Outline each Plasmodium falciparum-infected red blood cell.
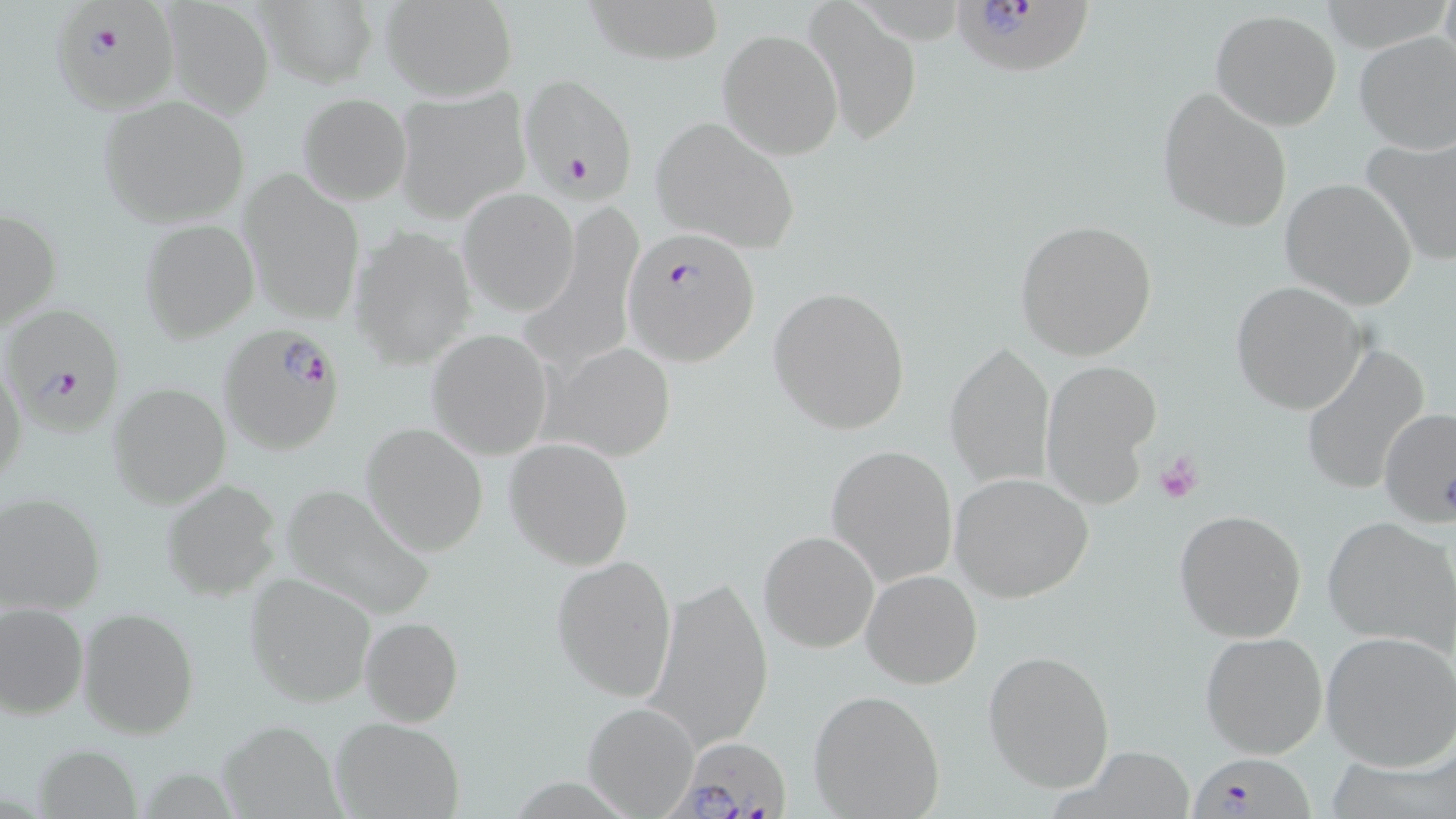

Approximate bounding boxes as named x1/y1/x2/y2 corners in pixels.
Plasmodium falciparum-infected red blood cells: (x1=55, y1=2, x2=186, y2=121), (x1=949, y1=4, x2=1094, y2=78), (x1=528, y1=78, x2=635, y2=210), (x1=622, y1=226, x2=762, y2=368), (x1=4, y1=306, x2=127, y2=427), (x1=217, y1=324, x2=346, y2=455), (x1=660, y1=735, x2=792, y2=819), (x1=1191, y1=752, x2=1309, y2=819).

slide_level_diagnosis: Plasmodium falciparum
stain: May-Grünwald-Giemsa
modality: light microscopy
image_size: 1456×819 pixels
magnification: 1000x
field_of_view: one of a larger specimen
preparation: thin blood film
uninfected_red_blood_cell_locations: 'approximate bounding boxes as named x1/y1/x2/y2 corners in pixels: (x1=161, y1=0, x2=275, y2=118), (x1=583, y1=0, x2=725, y2=65), (x1=379, y1=1, x2=518, y2=100), (x1=804, y1=1, x2=924, y2=146), (x1=252, y1=2, x2=377, y2=87), (x1=1210, y1=8, x2=1342, y2=131), (x1=718, y1=28, x2=841, y2=159), (x1=1353, y1=31, x2=1456, y2=156), (x1=1157, y1=87, x2=1293, y2=233), (x1=394, y1=89, x2=530, y2=223), (x1=297, y1=92, x2=411, y2=206), (x1=98, y1=96, x2=248, y2=229), (x1=650, y1=115, x2=800, y2=253), (x1=1362, y1=133, x2=1456, y2=268), (x1=238, y1=171, x2=366, y2=325), (x1=1280, y1=178, x2=1417, y2=309), (x1=458, y1=187, x2=579, y2=315), (x1=1, y1=205, x2=61, y2=335), (x1=1014, y1=218, x2=1158, y2=362), (x1=138, y1=220, x2=259, y2=342), (x1=350, y1=225, x2=477, y2=367), (x1=1230, y1=281, x2=1368, y2=414), (x1=768, y1=286, x2=911, y2=435), (x1=427, y1=330, x2=554, y2=458), (x1=945, y1=341, x2=1055, y2=487), (x1=544, y1=342, x2=677, y2=464), (x1=1301, y1=342, x2=1433, y2=497), (x1=0, y1=354, x2=27, y2=495), (x1=1043, y1=362, x2=1163, y2=506), (x1=107, y1=381, x2=231, y2=509), (x1=1378, y1=407, x2=1456, y2=527), (x1=360, y1=422, x2=488, y2=555), (x1=505, y1=437, x2=635, y2=570), (x1=826, y1=444, x2=957, y2=587), (x1=950, y1=472, x2=1094, y2=601), (x1=161, y1=479, x2=282, y2=601), (x1=279, y1=483, x2=431, y2=620), (x1=1, y1=492, x2=105, y2=615), (x1=1173, y1=508, x2=1307, y2=642), (x1=1322, y1=517, x2=1456, y2=651), (x1=759, y1=530, x2=879, y2=653), (x1=553, y1=554, x2=678, y2=702), (x1=862, y1=568, x2=982, y2=689), (x1=245, y1=574, x2=375, y2=707), (x1=647, y1=576, x2=772, y2=752), (x1=0, y1=602, x2=87, y2=719), (x1=77, y1=608, x2=198, y2=738), (x1=359, y1=616, x2=464, y2=726), (x1=1321, y1=629, x2=1456, y2=771), (x1=1200, y1=631, x2=1330, y2=759), (x1=984, y1=648, x2=1116, y2=791), (x1=808, y1=689, x2=946, y2=818), (x1=582, y1=702, x2=699, y2=815), (x1=328, y1=716, x2=466, y2=819), (x1=216, y1=721, x2=344, y2=816), (x1=34, y1=745, x2=140, y2=818), (x1=1058, y1=749, x2=1195, y2=819)'
platelet_locations: 'approximate bounding boxes as named x1/y1/x2/y2 corners in pixels: (x1=1153, y1=449, x2=1205, y2=505)'